Identify the parasite.
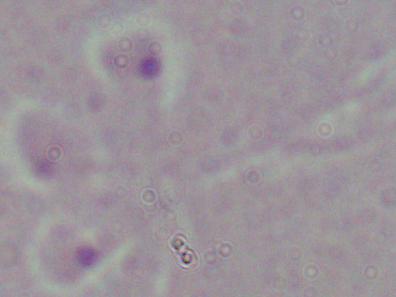

This is Leishmania.

{
  "modality": "photomicrograph",
  "magnification": "1000x"
}